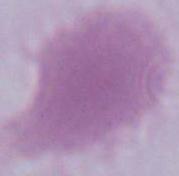

Captured at 1000x magnification. An erythrocyte is shown. Photomicrograph.